Locate every Plasmodium parasite.
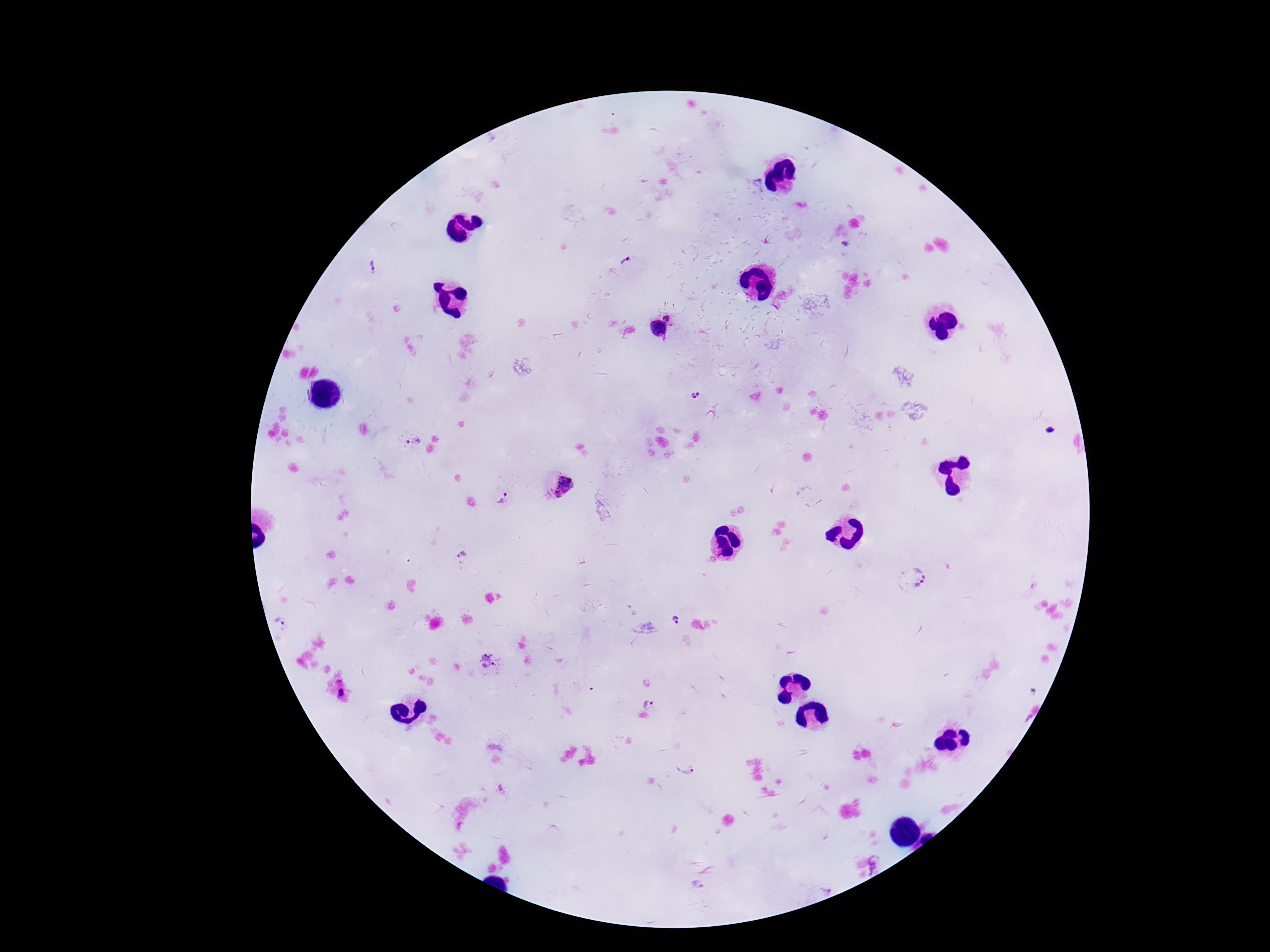

Approximate centers as {x, y} in pixels.
Plasmodium parasites: {760, 186}, {627, 262}, {372, 268}, {666, 316}, {658, 329}, {695, 395}, {413, 440}, {566, 482}, {557, 495}, {503, 500}, {464, 554}, {915, 577}, {675, 620}, {282, 624}, {489, 660}, {647, 703}, {685, 767}, {501, 788}, {697, 886}, {825, 887}.

Summary:
  - Capture: smartphone camera through the microscope eyepiece
  - Image size: 1270×952 pixels
  - Patient malaria status: positive
  - Preparation: thick blood film
  - Stain: Giemsa
  - Magnification: 100x
  - Field of view: single